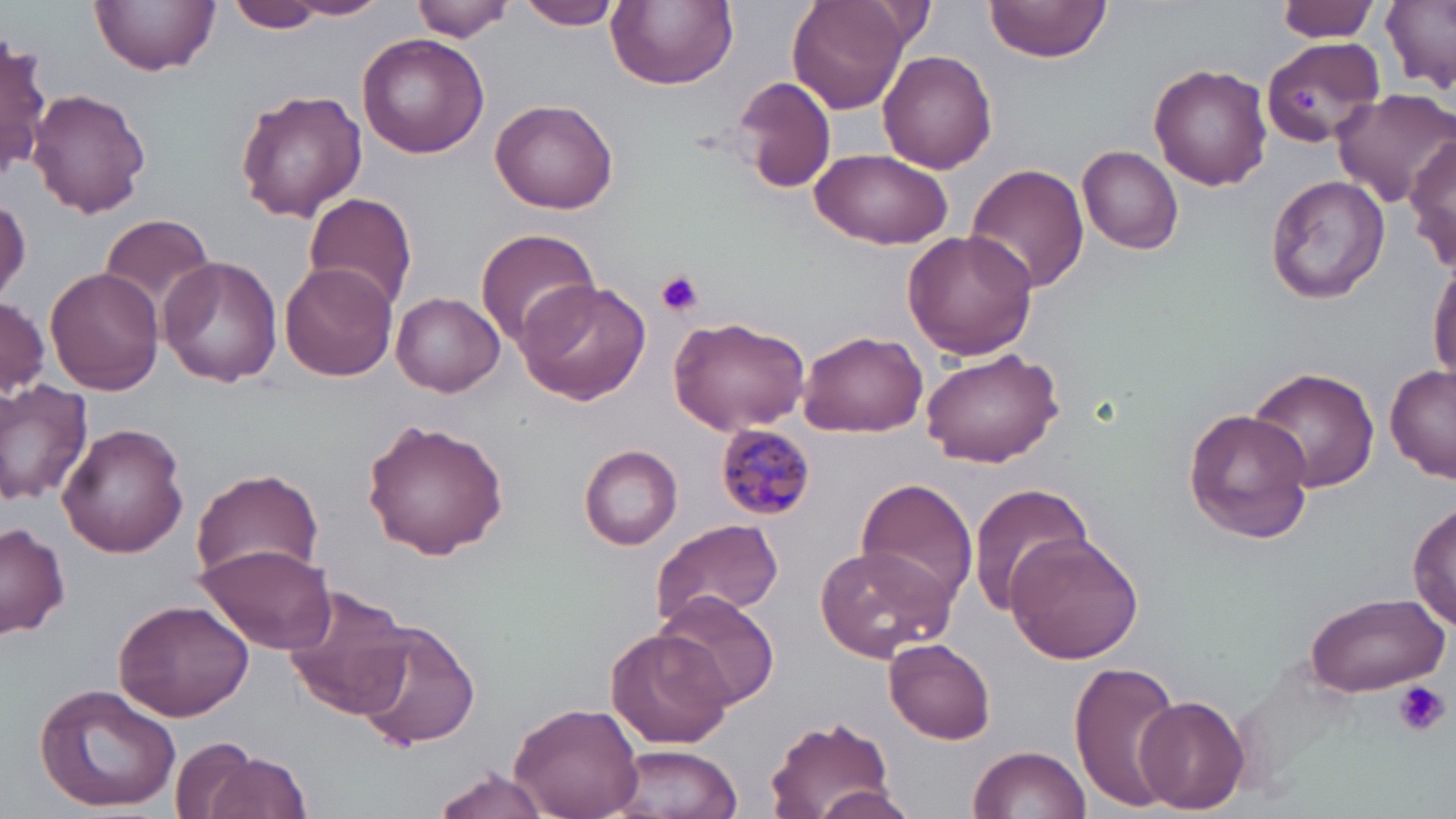
Summary:
  - Coordinate format: approximate bounding boxes as (x1,y1)-(x2,y2) corner pairs in pixels
  - Plasmodium malariae-infected red blood cell locations: (717,424)-(814,519)
  - Uninfected red blood cell locations: (92,0)-(219,75), (227,0)-(322,33), (284,0)-(395,19), (516,0)-(624,30), (607,0)-(738,89), (790,0)-(910,113), (984,0)-(1114,69), (1276,0)-(1380,42), (409,1)-(517,42), (1381,1)-(1456,94), (864,3)-(936,47), (358,32)-(489,159), (1,34)-(49,181), (1261,36)-(1385,148), (879,49)-(998,174), (1147,62)-(1272,191), (732,74)-(837,193), (1331,86)-(1456,210), (30,89)-(150,216), (234,89)-(367,221), (489,98)-(622,215), (1407,135)-(1456,269), (1078,145)-(1186,254), (810,149)-(952,251), (964,163)-(1090,297), (1264,174)-(1390,304), (303,192)-(418,312), (0,194)-(32,304), (97,212)-(218,317), (474,227)-(600,349), (903,229)-(1039,361), (158,256)-(283,388), (1429,258)-(1456,384), (279,261)-(397,384), (43,267)-(163,395), (514,279)-(651,406), (391,292)-(506,397), (1,296)-(48,400), (667,315)-(812,435), (800,328)-(929,438), (918,344)-(1063,467), (1385,363)-(1456,481), (1247,366)-(1381,493), (0,379)-(95,504), (1181,408)-(1316,542), (362,418)-(511,561), (57,421)-(188,558), (579,443)-(682,548), (188,467)-(327,586), (855,476)-(979,615), (965,482)-(1095,614), (1410,502)-(1455,632), (650,517)-(784,630), (0,521)-(71,641), (1005,532)-(1144,665), (194,541)-(335,656), (814,544)-(954,663), (136,563)-(283,693), (281,583)-(415,722), (1302,590)-(1448,697), (653,592)-(780,710), (113,598)-(255,720), (353,618)-(481,751), (607,626)-(734,750), (884,639)-(996,744), (1070,659)-(1184,812), (33,681)-(182,813), (1134,694)-(1249,813), (508,699)-(647,819), (763,715)-(895,819), (170,733)-(268,819), (605,744)-(743,819), (968,745)-(1090,818), (200,752)-(314,819), (428,766)-(554,819), (812,787)-(920,819)
  - Platelet locations: (1291,85)-(1317,114), (656,271)-(702,316), (1393,681)-(1450,737)
  - Slide-level diagnosis: Plasmodium malariae
  - Preparation: thin blood film
  - Image size: 1456×819 pixels
  - Magnification: 1000x
  - Stain: May-Grünwald-Giemsa
  - Modality: optical microscopy
  - Field of view: one of a larger specimen